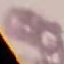
malaria_status: uninfected
image_type: cell patch, automatically extracted from a larger field of view and resized to 64 × 64 pixels
stain: Giemsa
capture: smartphone camera at the microscope eyepiece
preparation: thin smear